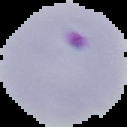
Summary:
  - Image type: segmented cell region on a black background
  - Image size: 127×127 pixels
  - Result: Plasmodium parasites identified
  - Preparation: thin blood smear